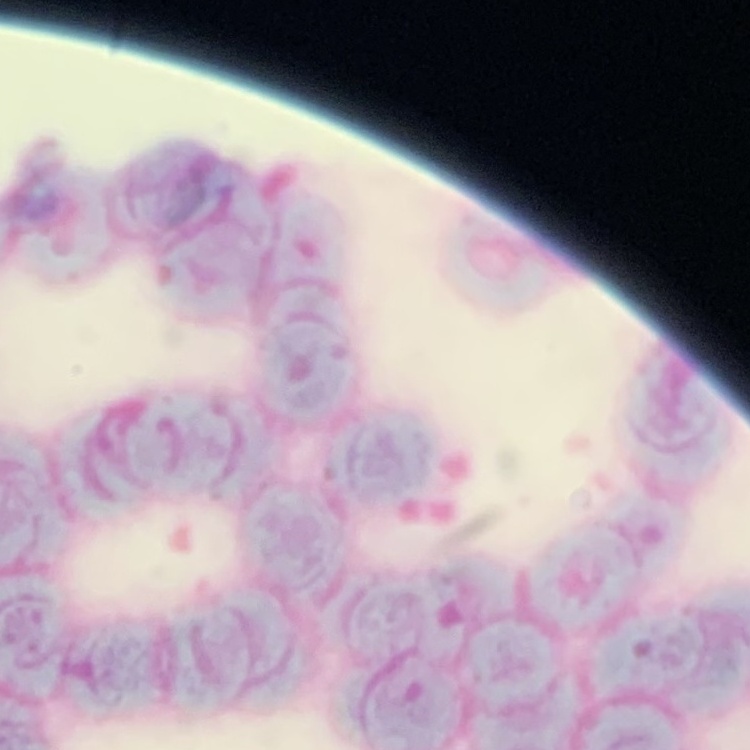

erythrocyte morphology = rouleaux formation
preparation = thin blood film
stain = Field's or Giemsa
image type = square crop of a larger photomicrograph